Outline each Plasmodium ovale-infected red blood cell.
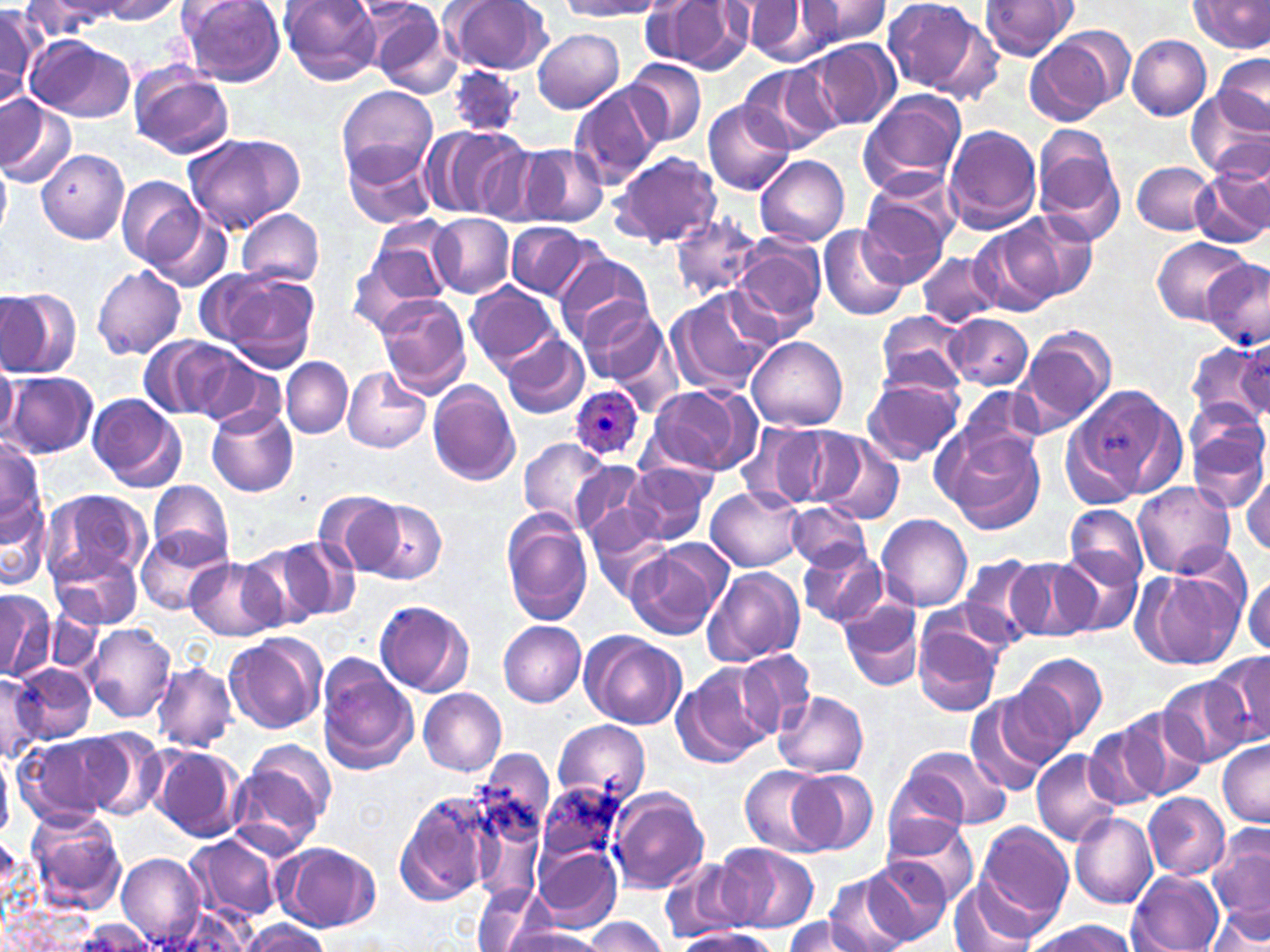
Approximate bounding boxes as (x1, y1, x2, y2) in pixels.
Plasmodium ovale-infected red blood cells: (568, 385, 645, 462).

slide-level diagnosis = Plasmodium ovale
magnification = 1000x
stain = May-Grünwald-Giemsa
field of view = one of a larger specimen
uninfected red blood cell locations = approximate bounding boxes as (x1, y1, x2, y2) in pixels: (92, 0, 186, 24), (177, 0, 287, 86), (280, 0, 383, 84), (443, 0, 553, 76), (797, 0, 892, 47), (881, 0, 998, 99), (1190, 0, 1269, 53), (560, 1, 663, 19), (743, 1, 843, 66), (979, 1, 1079, 60), (23, 2, 126, 36), (642, 2, 751, 72), (0, 4, 45, 100), (368, 4, 463, 99), (532, 27, 625, 114), (1024, 33, 1123, 126), (1125, 33, 1212, 120), (26, 36, 135, 121), (805, 40, 899, 130), (1213, 53, 1270, 133), (622, 58, 707, 148), (446, 64, 526, 136), (738, 65, 839, 155), (129, 68, 232, 159), (567, 84, 663, 190), (335, 85, 440, 187), (1188, 90, 1270, 181), (857, 91, 967, 196), (0, 96, 75, 187), (702, 98, 797, 196), (1032, 123, 1125, 243), (418, 124, 527, 219), (943, 124, 1043, 233), (182, 133, 303, 234), (515, 142, 608, 229), (343, 143, 438, 231), (474, 144, 551, 227), (37, 149, 127, 243), (609, 151, 723, 250), (755, 156, 849, 245), (0, 161, 11, 239), (1132, 161, 1220, 235), (1191, 168, 1270, 246), (117, 176, 204, 271), (856, 179, 958, 285), (139, 206, 234, 294), (236, 209, 324, 287), (999, 211, 1096, 305), (430, 213, 515, 298), (668, 215, 765, 302), (364, 219, 458, 309), (507, 222, 597, 299), (818, 224, 911, 323), (971, 225, 1064, 317), (730, 233, 828, 337), (1153, 237, 1250, 324), (915, 251, 1000, 324), (555, 253, 654, 338), (1201, 260, 1270, 349), (90, 266, 186, 360), (215, 271, 320, 371), (465, 282, 560, 370), (0, 287, 79, 378), (666, 288, 776, 396), (374, 294, 471, 397), (577, 301, 666, 386), (873, 312, 971, 398), (946, 313, 1034, 390), (1017, 324, 1118, 432), (500, 333, 591, 420), (141, 335, 248, 423), (747, 336, 849, 432), (1234, 337, 1269, 417), (1187, 340, 1270, 429), (0, 358, 17, 443), (282, 358, 352, 438), (200, 363, 285, 436), (341, 365, 432, 453), (4, 371, 98, 459), (863, 375, 964, 466), (427, 381, 520, 485), (1065, 383, 1182, 504), (646, 384, 760, 476), (954, 387, 1049, 471), (85, 394, 185, 492), (1191, 394, 1264, 475), (207, 407, 297, 497), (763, 423, 856, 507), (1188, 423, 1269, 514), (938, 425, 1045, 534), (816, 436, 906, 527), (0, 438, 46, 544), (517, 438, 609, 527), (569, 459, 651, 543), (624, 462, 715, 546), (1241, 470, 1270, 557), (1133, 480, 1235, 578), (148, 481, 233, 565), (706, 487, 805, 571), (44, 489, 152, 585), (314, 490, 403, 574), (1, 496, 50, 593), (363, 501, 446, 585), (787, 502, 869, 571), (1063, 503, 1149, 592), (500, 509, 595, 627), (877, 514, 973, 611), (588, 516, 673, 601), (135, 530, 227, 615), (270, 535, 359, 622), (797, 542, 888, 629), (231, 545, 328, 631), (626, 546, 722, 640), (50, 547, 145, 629), (1057, 551, 1143, 635), (957, 555, 1047, 646), (184, 556, 284, 641), (1008, 558, 1103, 646), (703, 566, 806, 666), (1136, 566, 1246, 673), (1243, 573, 1270, 656), (0, 591, 50, 680), (840, 599, 925, 692), (375, 600, 473, 696), (45, 614, 100, 673), (499, 619, 587, 706), (913, 619, 1004, 717), (84, 622, 178, 722), (224, 632, 327, 734), (581, 633, 687, 729), (735, 651, 815, 738), (1020, 653, 1109, 744), (1208, 653, 1270, 752), (152, 661, 236, 752), (673, 663, 775, 765), (16, 664, 95, 745), (317, 667, 418, 774), (0, 673, 45, 760), (995, 676, 1090, 769), (1157, 677, 1250, 767), (419, 689, 506, 775), (774, 690, 869, 777), (963, 696, 1054, 797), (1116, 709, 1211, 801), (552, 719, 652, 805), (1083, 723, 1169, 813), (72, 728, 166, 819), (17, 733, 124, 824), (238, 740, 336, 844), (1218, 740, 1268, 828), (901, 744, 1012, 831), (150, 746, 245, 842), (0, 749, 13, 837), (474, 750, 557, 848), (1032, 750, 1123, 847), (740, 765, 831, 856), (881, 765, 971, 853), (787, 768, 876, 855), (534, 782, 630, 869), (394, 789, 501, 908), (610, 789, 709, 896), (1142, 793, 1230, 879), (25, 809, 126, 915), (1069, 810, 1158, 909), (884, 817, 981, 904), (976, 820, 1074, 927), (1209, 825, 1269, 928), (185, 837, 279, 924), (277, 843, 380, 932), (720, 844, 819, 933), (533, 846, 622, 931), (117, 852, 206, 947), (867, 856, 955, 945), (661, 859, 750, 943), (1127, 870, 1223, 952), (821, 874, 914, 952), (951, 879, 1042, 952), (473, 882, 549, 952), (1207, 901, 1268, 951), (156, 906, 259, 952), (675, 912, 774, 945), (783, 917, 877, 952), (585, 918, 667, 952), (1024, 918, 1141, 952), (238, 919, 329, 952), (80, 920, 154, 952), (504, 927, 607, 952), (673, 928, 777, 952)
preparation = thin blood film
image size = 1270×952 pixels
modality = optical microscopy